Comment on the morphology of the red blood cells.
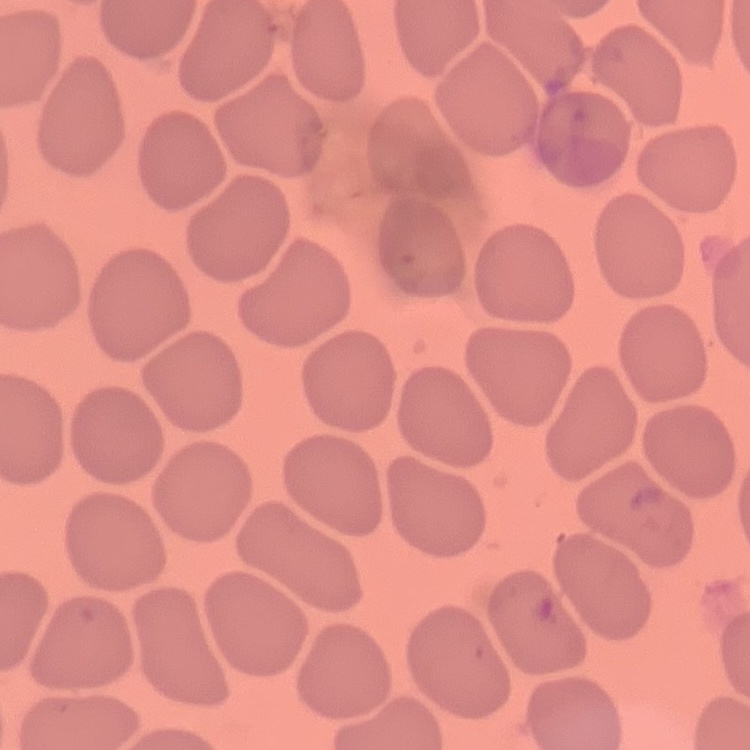

They show no rouleaux formation.

stain = Field's or Giemsa
preparation = thin peripheral smear
image type = one tile cut from a larger photomicrograph